Describe the morphology of the erythrocytes.
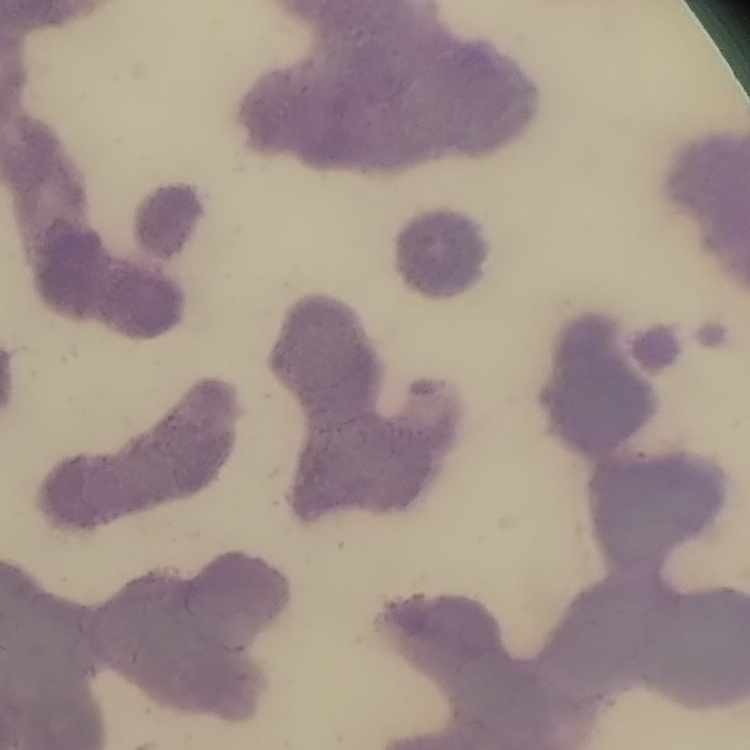

They show rouleaux formation.

stain = Field's or Giemsa
image type = one tile cut from a larger photomicrograph
preparation = thin blood smear